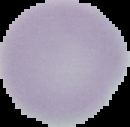

From a thin blood film. Image is 130×127 pixels. Segmented cell region on a black background. Result: no malaria parasites detected.